Locate every blood parasite and identify its species.
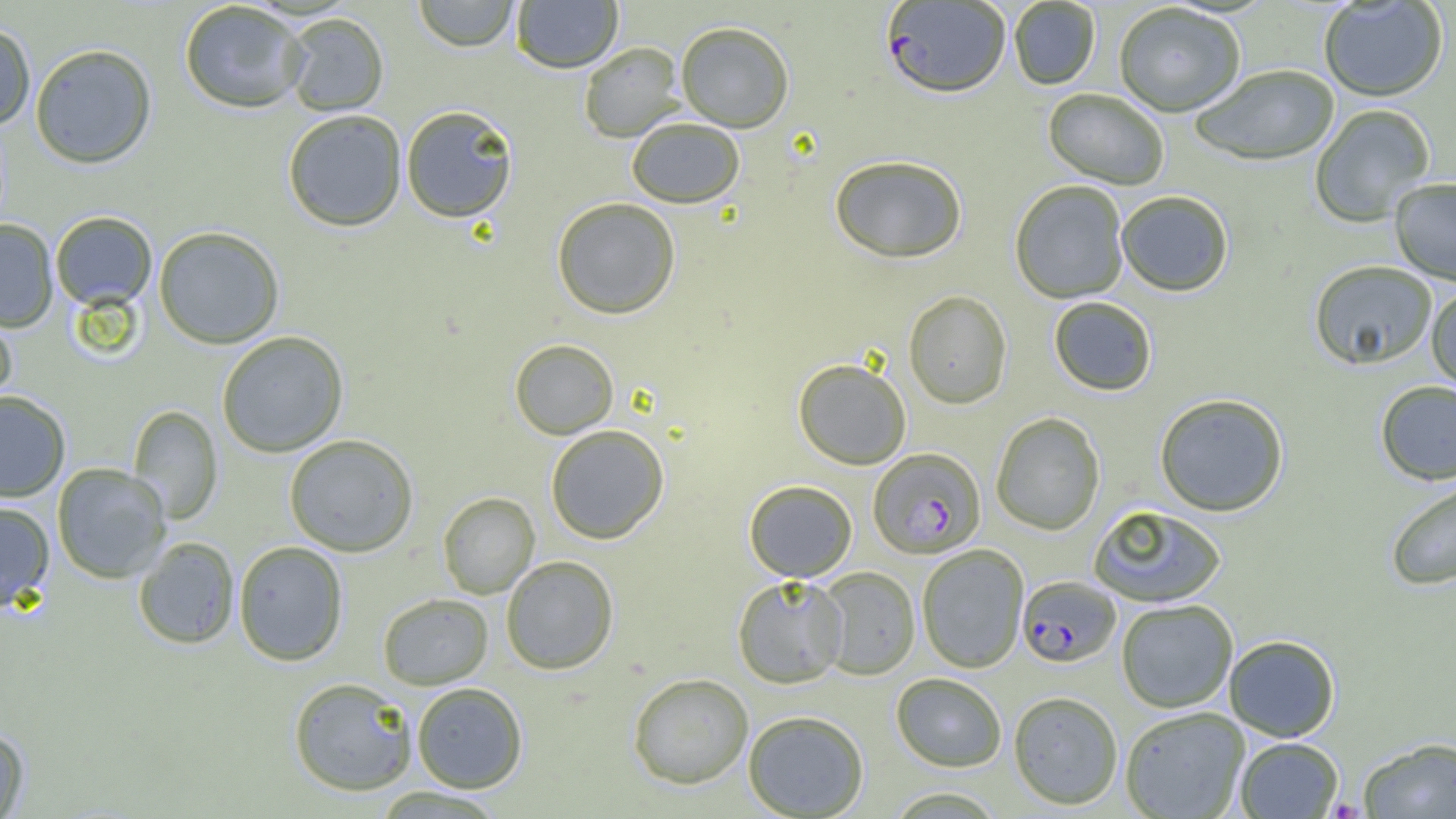

Approximate bounding boxes as (x1,y1)-(x2,y2) corner pairs in pixels.
Plasmodium falciparum-infected red blood cells: (881,1)-(1010,101), (868,448)-(986,560), (1017,576)-(1121,667).
No Plasmodium ovale, Plasmodium malariae, Plasmodium vivax, Babesia divergens, or Trypanosoma brucei observed.

slide-level diagnosis = Plasmodium falciparum
magnification = 1000x
field of view = single
preparation = thin blood smear
uninfected red blood cell locations = approximate bounding boxes as (x1,y1)-(x2,y2) corner pairs in pixels: (412,0)-(520,52), (511,1)-(623,74), (1009,1)-(1100,91), (1319,1)-(1447,103), (179,2)-(308,114), (1114,5)-(1246,119), (282,13)-(389,117), (676,22)-(794,133), (0,23)-(36,129), (578,42)-(685,143), (30,43)-(157,169), (1192,67)-(1339,167), (1043,89)-(1168,190), (401,105)-(518,224), (1309,105)-(1435,228), (283,111)-(407,233), (627,119)-(745,209), (829,156)-(967,266), (1389,178)-(1456,286), (1010,181)-(1129,305), (1116,192)-(1233,298), (552,198)-(681,320), (50,212)-(157,311), (0,220)-(59,333), (154,226)-(284,349), (1309,262)-(1437,371), (1426,287)-(1456,393), (903,291)-(1012,409), (1049,297)-(1157,397), (0,309)-(17,416), (216,331)-(349,458), (509,340)-(619,440), (793,359)-(911,470), (1375,381)-(1456,486), (0,390)-(71,502), (1154,393)-(1289,517), (128,405)-(223,525), (991,413)-(1105,536), (545,425)-(670,544), (284,434)-(419,557), (52,463)-(171,584), (1384,477)-(1456,592), (744,480)-(857,582), (438,492)-(540,599), (0,500)-(55,612), (1088,504)-(1227,608), (133,537)-(240,649), (233,541)-(349,666), (916,545)-(1029,673), (501,556)-(619,675), (815,567)-(920,680), (732,575)-(849,688), (378,593)-(493,690), (1116,600)-(1238,713), (1224,634)-(1340,742), (627,672)-(753,789), (891,673)-(1007,772), (288,677)-(418,797), (412,682)-(528,793), (1008,691)-(1123,810), (1120,706)-(1250,819), (743,711)-(869,818), (0,726)-(30,818), (1235,737)-(1343,818), (1359,737)-(1456,818), (370,787)-(508,817), (884,787)-(1008,818)
modality = optical microscopy
image size = 1456×819 pixels